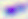 Toxoplasma gondii is shown. Micrograph. 400x magnification.